Identify the parasite.
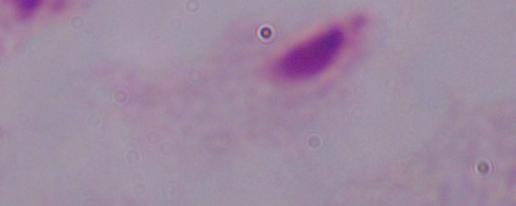

A trichomonad.

{
  "magnification": "1000x",
  "modality": "photomicrograph"
}